Name the parasite shown.
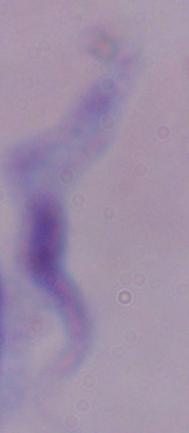
This is a trypanosome.

Summary:
  - Magnification: 1000x
  - Modality: micrograph